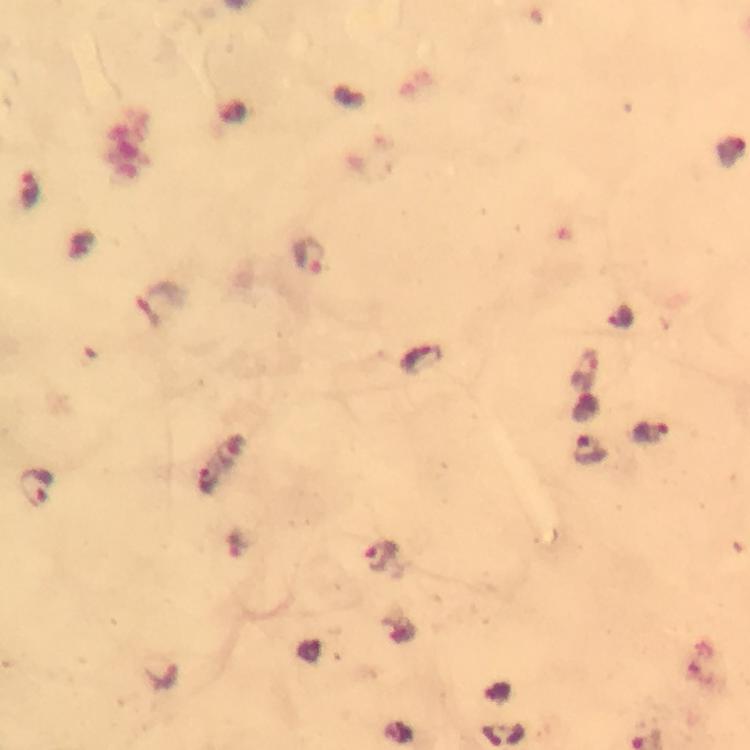

cropped from = a single field of view
capture = smartphone mounted on the microscope
preparation = thick blood smear
image size = 750×750 pixels
context = from a malaria diagnostic workup
malaria parasite locations = approximate centers as [x, y] in pixels: [28, 189], [310, 256], [422, 357], [591, 448], [212, 476], [37, 488], [379, 558]
immersion oil = used
stain = Giemsa
magnification = 100x